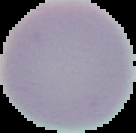
Summary:
  - Preparation: thin blood smear
  - Image type: segmented cell region on a black background
  - Malaria status: uninfected
  - Image size: 136×133 pixels